Comment on the morphology of the red blood cells.
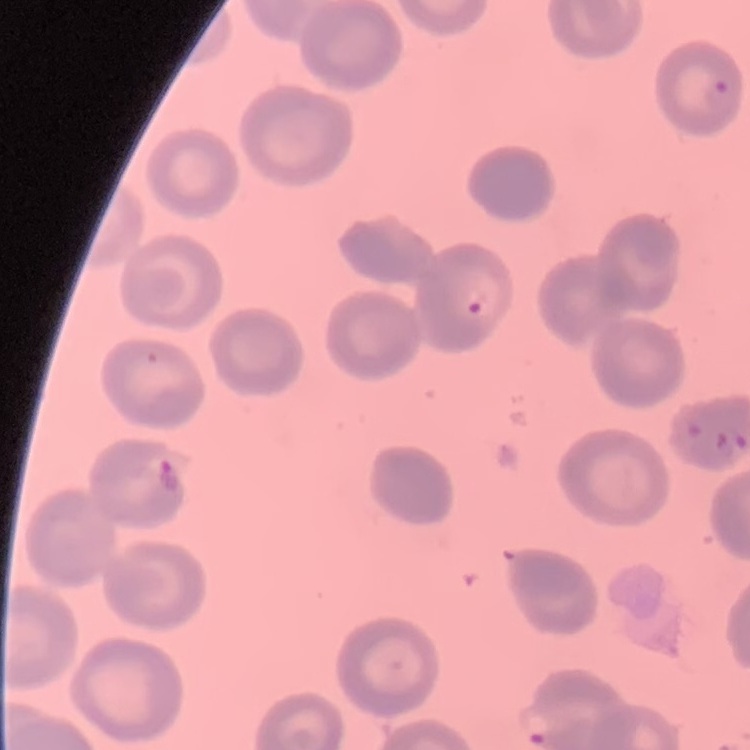
They show no rouleaux formation.

Summary:
  - Image type: square crop of a larger photomicrograph
  - Stain: Field's or Giemsa
  - Preparation: thin peripheral smear